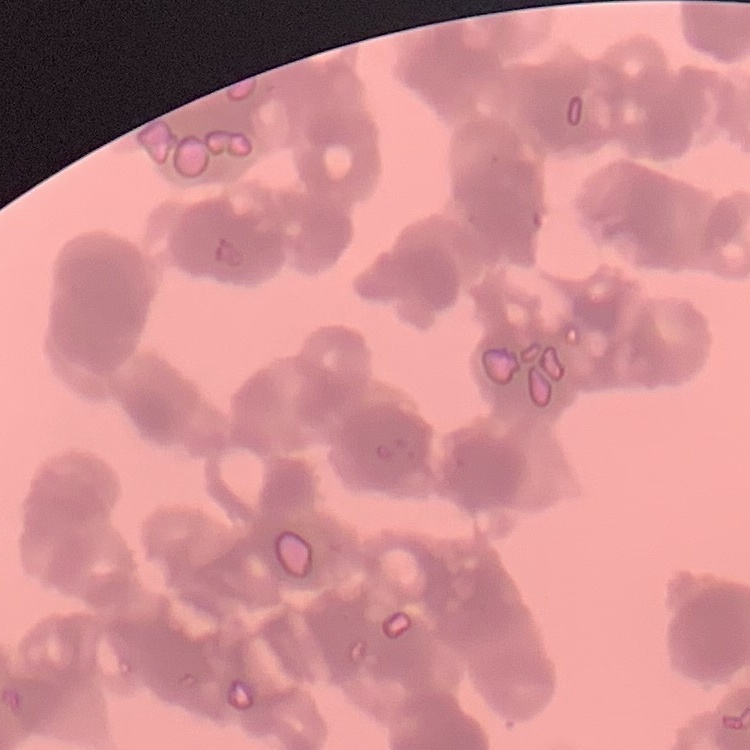
red blood cell morphology = rouleaux formation
stain = Field's or Giemsa
image type = one tile cut from a larger photomicrograph
preparation = thin peripheral smear